Classify this cell by malaria status.
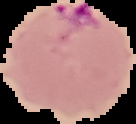
It is parasitized.

From a thin blood smear. Image is 136×124 pixels. Segmented cell region on a black background.